Identify the blood parasite species.
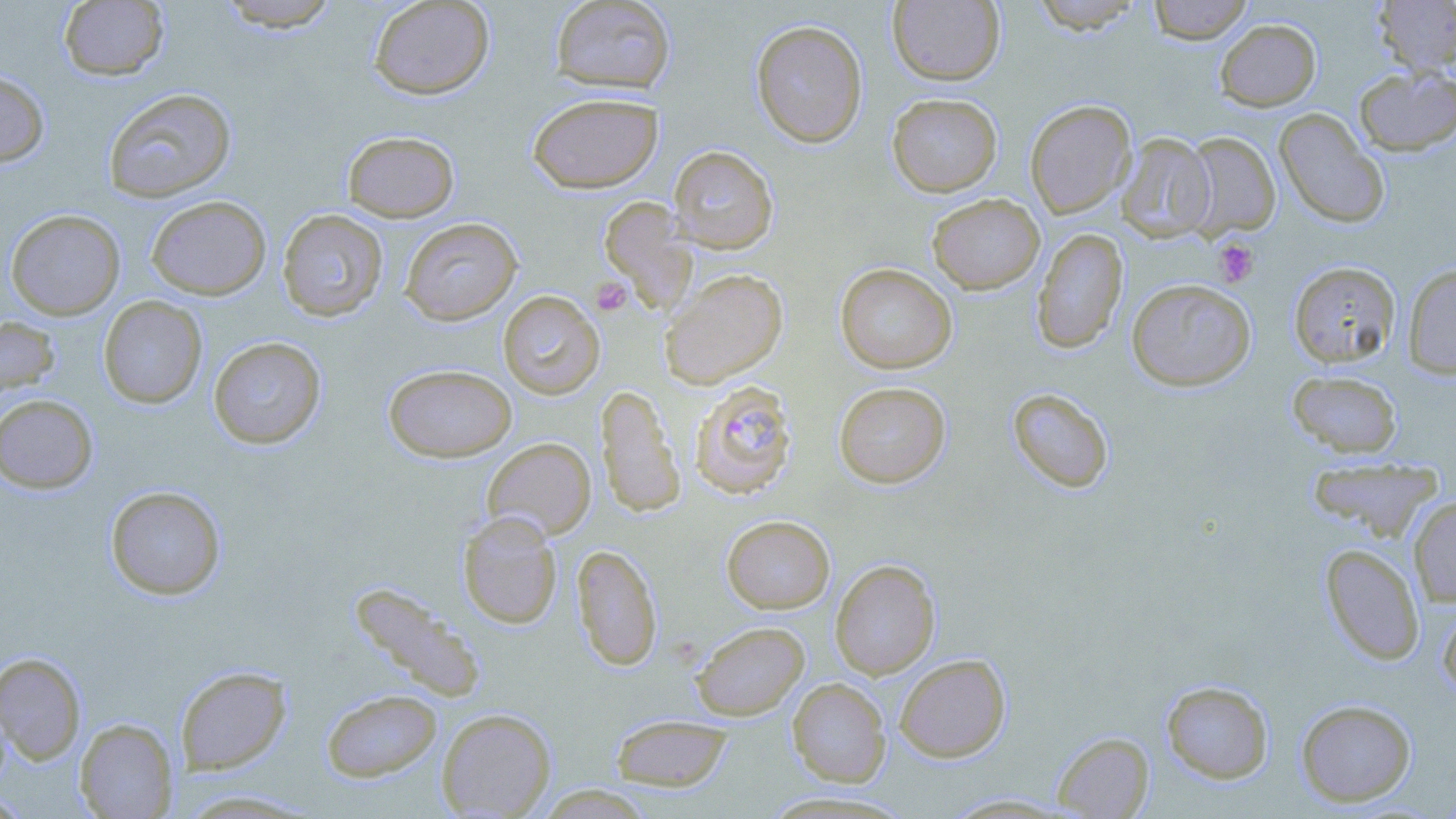

Plasmodium falciparum.

Approximate bounding boxes as (x1, y1, x2, y2) in pixels. Platelet locations: (1213, 238, 1260, 288), (589, 277, 632, 317). Plasmodium falciparum-infected red blood cell locations: (689, 380, 798, 499). Uninfected red blood cell locations: (59, 0, 168, 81), (215, 0, 343, 31), (368, 0, 495, 99), (549, 0, 676, 95), (1026, 0, 1149, 34), (1147, 0, 1254, 44), (1373, 0, 1456, 77), (887, 1, 1005, 86), (1215, 18, 1321, 111), (750, 19, 868, 148), (1353, 66, 1456, 156), (0, 68, 50, 167), (102, 88, 236, 203), (527, 92, 664, 194), (887, 93, 1003, 197), (1025, 99, 1136, 219), (1274, 109, 1389, 229), (342, 130, 460, 222), (1183, 132, 1280, 237), (1117, 133, 1216, 242), (669, 145, 779, 254), (927, 193, 1045, 294), (146, 195, 271, 300), (599, 197, 697, 316), (6, 209, 125, 320), (277, 209, 389, 322), (399, 217, 522, 325), (1031, 227, 1128, 354), (1288, 261, 1401, 368), (835, 263, 957, 374), (1403, 263, 1456, 379), (660, 268, 788, 389), (1126, 278, 1256, 391), (498, 290, 605, 399), (98, 296, 207, 409), (0, 315, 60, 400), (208, 336, 327, 449), (383, 363, 517, 462), (1287, 370, 1403, 459), (833, 381, 951, 488), (595, 384, 685, 519), (1006, 388, 1115, 494), (0, 394, 98, 493), (482, 437, 596, 540), (1307, 457, 1442, 541), (105, 485, 226, 600), (1408, 495, 1456, 606), (457, 511, 563, 629), (721, 515, 835, 613), (571, 544, 662, 671), (1320, 544, 1425, 665), (830, 559, 940, 679), (349, 581, 488, 702), (1437, 597, 1456, 703), (691, 621, 810, 720), (0, 652, 86, 764), (894, 654, 1011, 762), (175, 666, 291, 774), (787, 678, 891, 787), (1161, 680, 1274, 784), (321, 689, 442, 782), (1296, 699, 1416, 806), (437, 708, 556, 818), (609, 714, 733, 791), (74, 718, 177, 818), (1052, 731, 1154, 818), (536, 785, 657, 819), (0, 791, 33, 818), (940, 793, 1077, 816). Thin blood film. Image is 1456×819 pixels. Single field of view. May-Grünwald-Giemsa-stained preparation. Optical microscopy. Captured at 1000x magnification.